Locate every Plasmodium parasite.
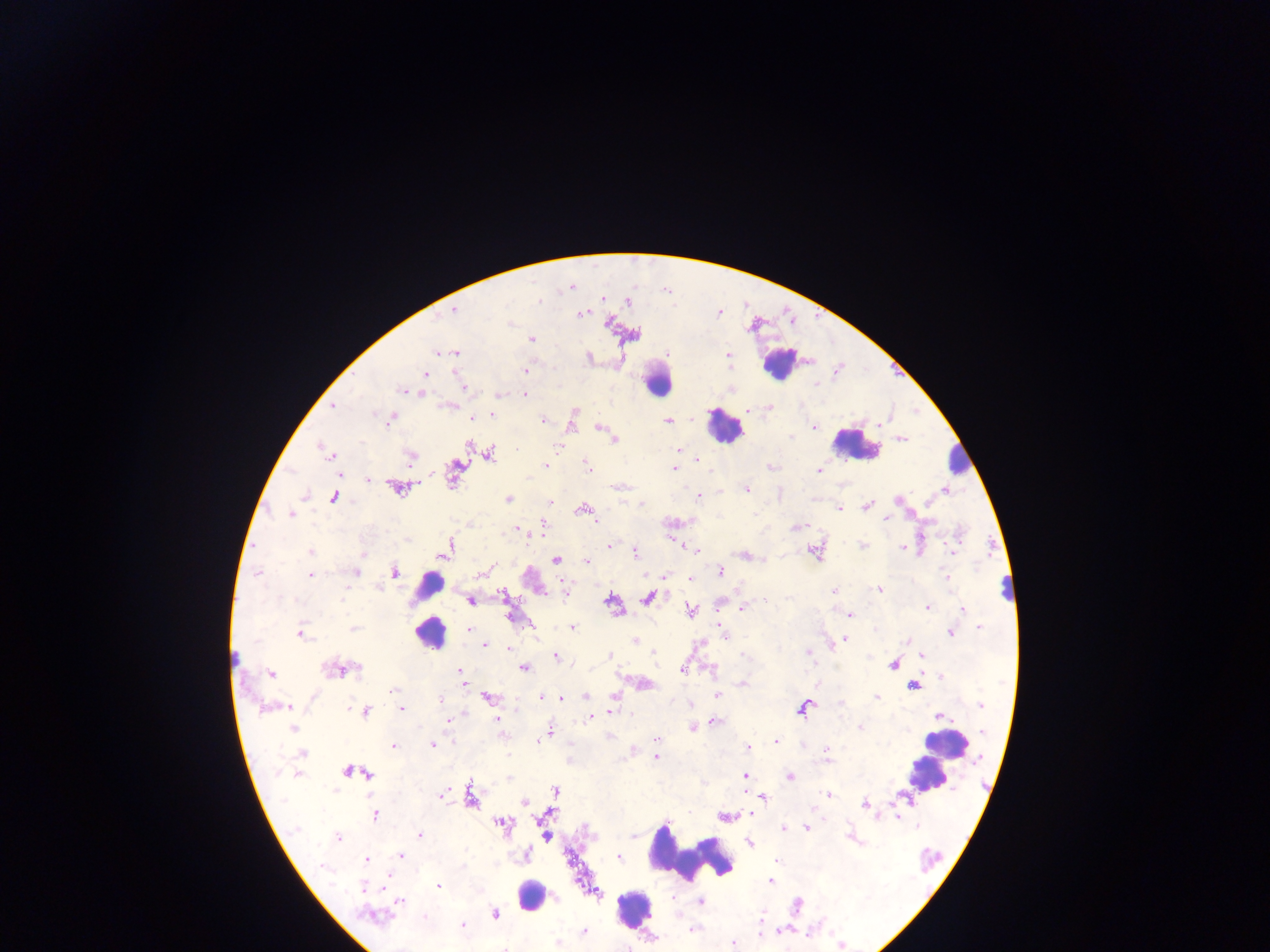
Approximate centers as [x, y] in pixels.
Plasmodium parasites: [571, 287], [602, 298], [539, 301], [628, 301], [454, 309], [581, 314], [511, 324], [532, 339], [437, 351], [456, 352], [728, 353], [525, 371], [425, 374], [463, 387], [401, 390], [498, 395], [525, 395], [332, 406], [770, 407], [748, 410], [574, 412], [374, 414], [492, 414], [471, 418], [391, 419], [542, 421], [668, 421], [813, 426], [600, 427], [790, 437], [615, 439], [903, 439], [558, 446], [323, 448], [678, 450], [328, 454], [490, 454], [410, 456], [697, 459], [546, 465], [455, 466], [588, 466], [674, 468], [819, 470], [369, 480], [397, 488], [746, 489], [945, 490], [305, 496], [699, 496], [334, 498], [508, 499], [897, 500], [550, 503], [642, 505], [868, 506], [839, 508], [583, 509], [290, 514], [886, 519], [801, 525], [542, 527], [518, 529], [408, 540], [863, 544], [610, 546], [448, 548], [903, 548], [697, 551], [310, 552], [952, 552], [635, 553], [362, 554], [556, 560], [586, 562], [720, 571], [355, 572], [394, 572], [481, 572], [257, 574], [311, 575], [690, 578], [947, 578], [379, 587], [879, 589], [834, 590], [502, 595], [647, 598], [470, 601], [611, 602], [767, 602], [927, 607], [743, 608], [962, 609], [691, 610], [850, 615], [354, 628], [572, 628], [979, 628], [469, 629], [875, 629], [950, 634], [300, 635], [845, 639], [635, 640], [906, 640], [485, 645], [832, 646], [508, 648], [654, 652], [808, 653], [609, 655], [555, 656], [921, 656], [892, 664], [358, 668], [334, 669], [525, 669], [683, 670], [461, 671], [271, 674], [941, 677], [462, 681], [645, 683], [742, 684], [913, 686], [393, 690], [717, 695], [585, 696], [614, 696], [488, 697], [876, 697], [541, 698], [561, 698], [440, 700], [982, 705], [288, 707], [802, 707], [263, 709], [401, 709], [365, 712], [612, 712], [939, 716], [589, 718], [497, 720], [448, 721], [715, 721], [860, 727], [693, 728], [292, 729], [551, 730], [983, 732], [656, 740], [776, 741], [538, 743], [432, 745], [393, 746], [747, 748], [827, 750], [302, 753], [655, 757], [348, 771], [369, 774], [744, 775], [789, 777], [555, 791], [828, 794], [441, 795], [763, 798], [470, 799], [524, 802], [865, 804], [750, 814], [375, 815], [502, 824], [917, 825], [784, 827], [806, 828], [295, 829], [420, 835], [547, 836], [338, 838], [749, 843], [401, 855], [527, 855], [619, 857], [367, 859], [776, 861], [324, 867], [771, 881], [439, 887], [363, 888], [596, 893], [399, 901], [701, 901], [495, 914], [375, 917], [425, 917], [462, 925], [692, 929], [584, 931], [557, 943], [732, 943], [842, 946].

Summary:
  - Leukocyte locations: [780, 364], [657, 381], [724, 426], [856, 446], [959, 461], [1008, 590], [425, 594], [430, 632], [947, 744], [929, 777], [691, 856], [530, 896], [634, 908]
  - Capture: mobile-phone photograph through a microscope
  - Preparation: thick blood smear
  - Country: Ghana
  - Image size: 1270×952 pixels
  - Field of view: single